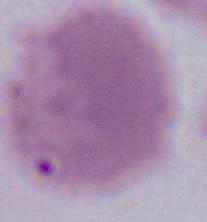
Summary:
  - Modality: photomicrograph
  - Magnification: 1000x
  - Identification: red blood cell